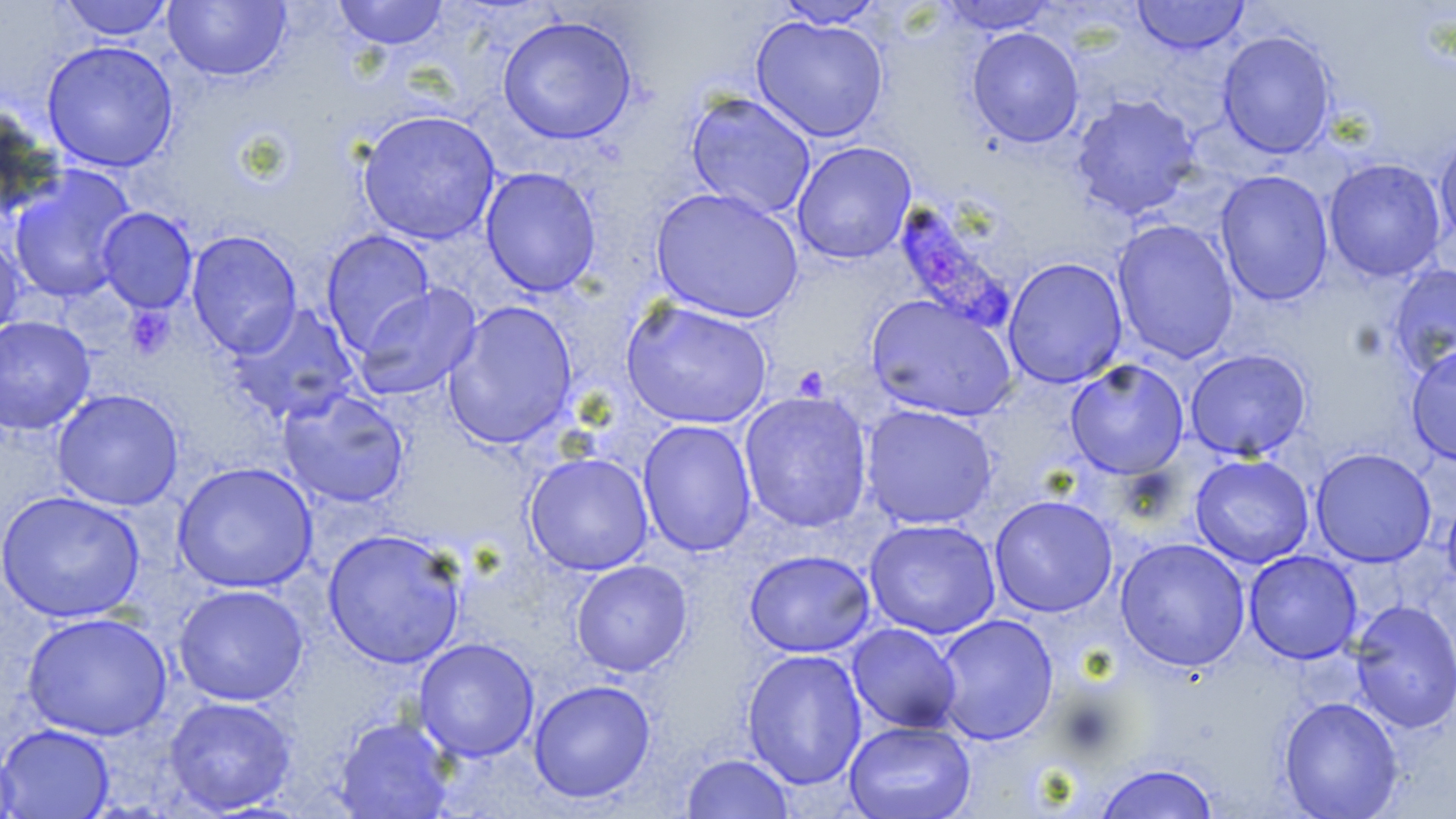

Approximate bounding boxes as (x1, y1, x2, y2) in pixels. Plasmodium falciparum-infected red blood cell locations: (893, 200, 1015, 330). Uninfected red blood cell locations: (57, 0, 175, 41), (334, 0, 449, 50), (1133, 0, 1249, 54), (163, 1, 291, 81), (775, 1, 884, 29), (938, 1, 1059, 35), (497, 15, 637, 144), (750, 15, 888, 143), (966, 26, 1085, 148), (1217, 30, 1337, 159), (41, 40, 179, 173), (685, 91, 817, 220), (1070, 94, 1201, 220), (0, 104, 62, 221), (357, 110, 501, 246), (1434, 132, 1456, 251), (791, 141, 917, 264), (1323, 158, 1446, 282), (480, 166, 601, 297), (8, 167, 136, 304), (1214, 170, 1334, 306), (650, 187, 804, 324), (96, 207, 198, 313), (1112, 218, 1240, 364), (186, 230, 303, 357), (320, 230, 436, 355), (0, 232, 24, 346), (1003, 256, 1128, 389), (1387, 263, 1456, 380), (353, 283, 482, 400), (865, 293, 1020, 422), (621, 298, 773, 429), (442, 300, 579, 450), (225, 302, 360, 425), (0, 315, 95, 434), (1406, 345, 1456, 466), (1185, 348, 1312, 462), (1065, 359, 1190, 479), (277, 388, 410, 508), (52, 389, 184, 511), (738, 391, 874, 533), (860, 403, 997, 529), (637, 419, 758, 557), (1310, 447, 1436, 567), (524, 452, 654, 576), (1190, 454, 1314, 568), (172, 461, 318, 593), (1, 489, 147, 623), (989, 495, 1118, 617), (1442, 495, 1456, 595), (863, 517, 1001, 639), (322, 528, 467, 668), (1114, 537, 1251, 672), (744, 549, 876, 658), (1244, 550, 1362, 664), (571, 559, 692, 677), (173, 583, 309, 706), (1349, 599, 1456, 733), (21, 612, 173, 741), (933, 613, 1058, 745), (847, 622, 963, 733), (413, 637, 540, 762), (742, 648, 868, 790), (528, 679, 656, 803), (163, 695, 297, 815), (1278, 696, 1404, 818), (333, 715, 456, 818), (844, 720, 976, 819), (1, 724, 115, 818), (0, 741, 20, 819), (681, 753, 795, 818), (1093, 762, 1219, 819). Platelet locations: (125, 306, 174, 360). Slide-level diagnosis: Plasmodium falciparum. Captured at 1000x magnification. May-Grünwald-Giemsa-stained preparation. One field of a larger specimen. Thin blood film. Optical microscopy. Image is 1456×819 pixels.